Point out each Plasmodium parasite.
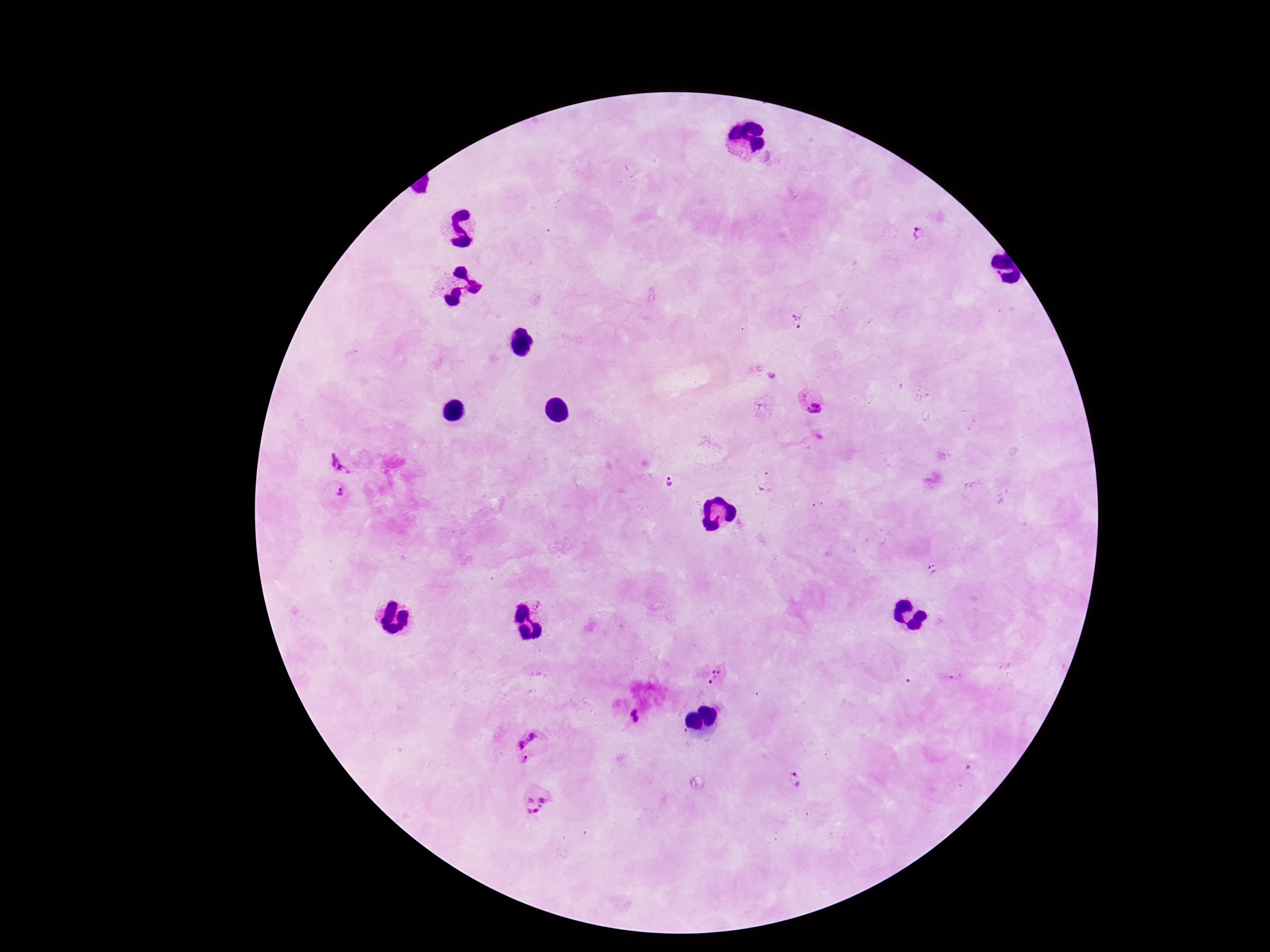

Approximate centers as [x, y] in pixels.
Plasmodium parasites: [918, 235], [798, 320], [814, 403], [344, 459], [671, 484], [340, 491], [935, 570], [715, 674], [952, 675], [539, 745], [796, 778], [535, 802].

Summary:
  - Stain: Giemsa
  - Preparation: thick blood film
  - Field of view: one from this slide
  - Patient malaria status: positive
  - Capture: smartphone camera through the microscope eyepiece
  - Image size: 1270×952 pixels
  - Magnification: 100x